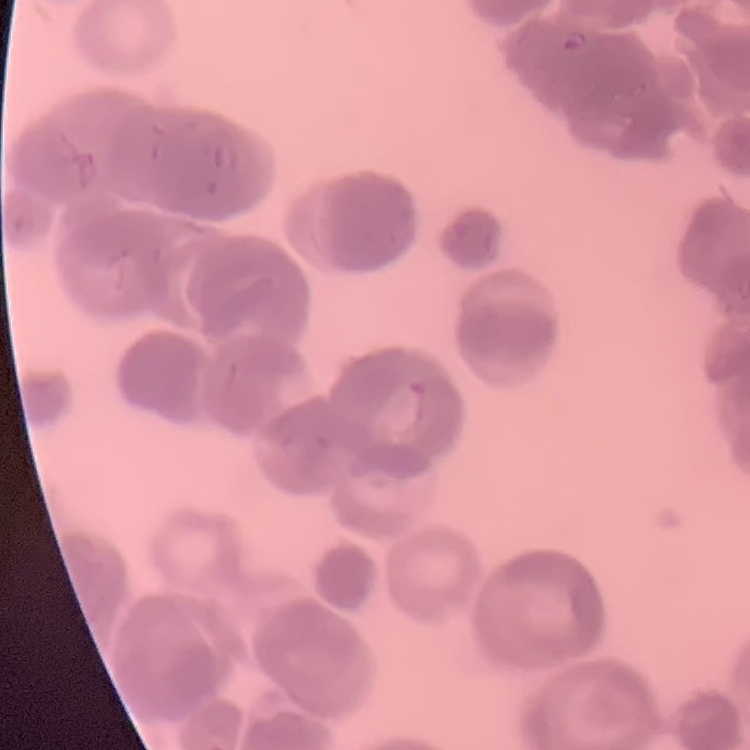
Summary:
  - Erythrocyte morphology: rouleaux formation
  - Image type: square crop of a larger photomicrograph
  - Stain: Field's or Giemsa
  - Preparation: thin peripheral smear